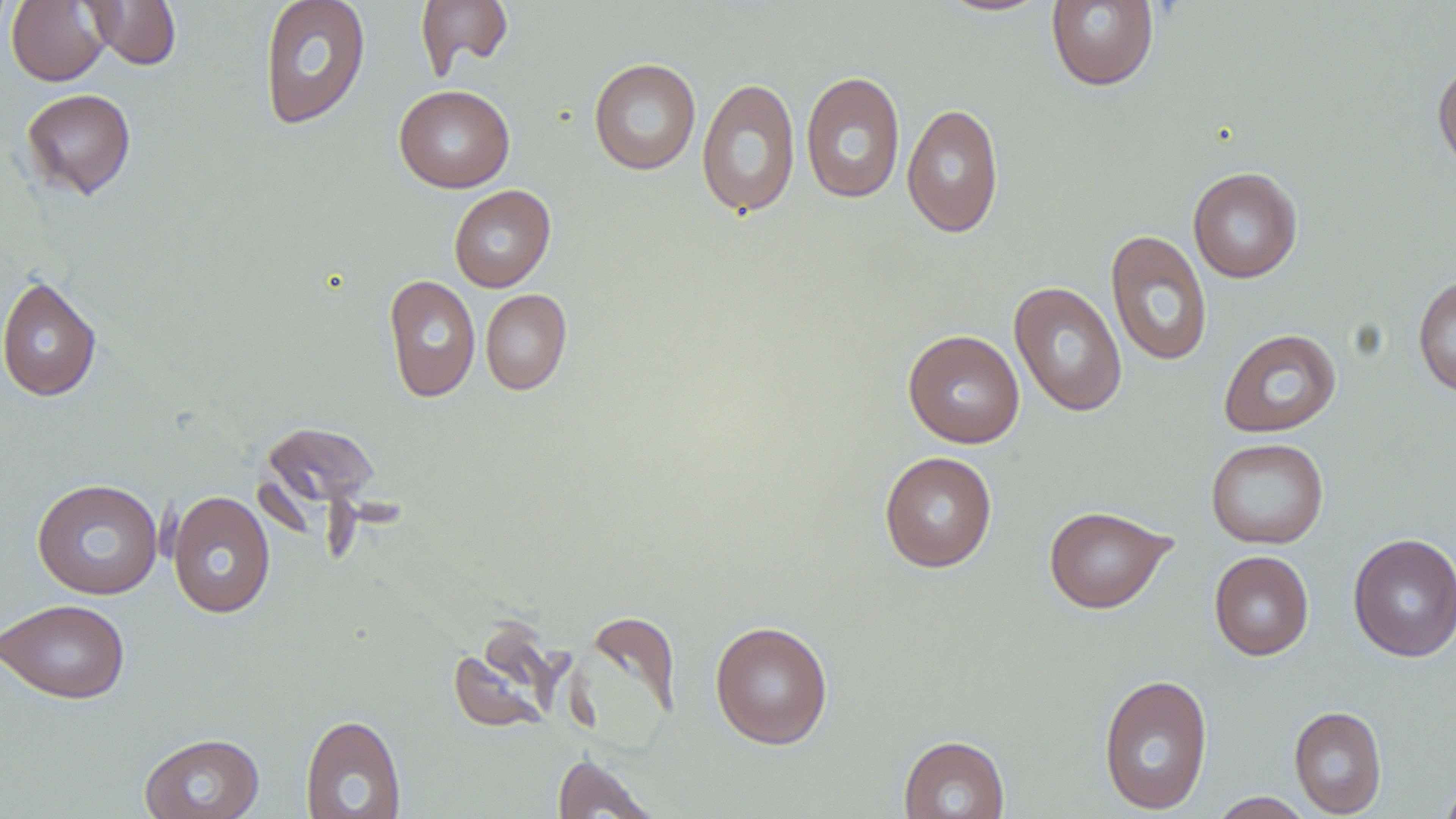
Summary:
  - Coordinate format: approximate bounding boxes as (x1,y1)-(x2,y2) corner pairs in pixels
  - Uninfected red blood cell locations: (6,0)-(111,86), (83,0)-(182,70), (258,0)-(371,130), (416,0)-(513,79), (932,0)-(1058,17), (1045,1)-(1159,91), (1432,57)-(1456,178), (588,58)-(701,175), (801,71)-(906,204), (696,78)-(802,218), (394,85)-(515,192), (21,88)-(136,200), (901,102)-(1004,239), (1188,167)-(1302,283), (449,185)-(556,292), (1106,230)-(1212,367), (383,274)-(480,402), (1412,274)-(1456,397), (0,275)-(102,401), (1009,281)-(1128,417), (480,289)-(572,395), (1218,328)-(1342,437), (903,330)-(1025,448), (261,420)-(381,511), (1205,438)-(1328,549), (879,451)-(997,572), (31,478)-(164,600), (167,490)-(276,619), (1043,505)-(1176,614), (1348,532)-(1456,662), (1209,550)-(1314,660), (1,598)-(131,703), (581,610)-(681,729), (710,620)-(833,749), (447,622)-(563,736), (1098,673)-(1213,815), (1289,705)-(1387,817), (300,714)-(406,818), (140,731)-(265,819), (898,734)-(1010,819), (552,753)-(661,818), (1438,775)-(1456,819), (1206,791)-(1316,818)
  - Slide-level diagnosis: no evidence of blood parasites
  - Stain: May-Grünwald-Giemsa
  - Image size: 1456×819 pixels
  - Preparation: thin blood film
  - Field of view: single
  - Modality: optical microscopy
  - Magnification: 1000x